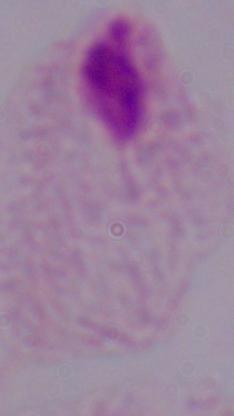
Photomicrograph. Captured at 1000x magnification. A trichomonad is seen.